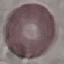
malaria status = uninfected
preparation = thin smear
capture = smartphone camera at the microscope eyepiece
image type = cell patch, automatically extracted from a larger field of view and resized to 64 × 64 pixels
stain = Giemsa